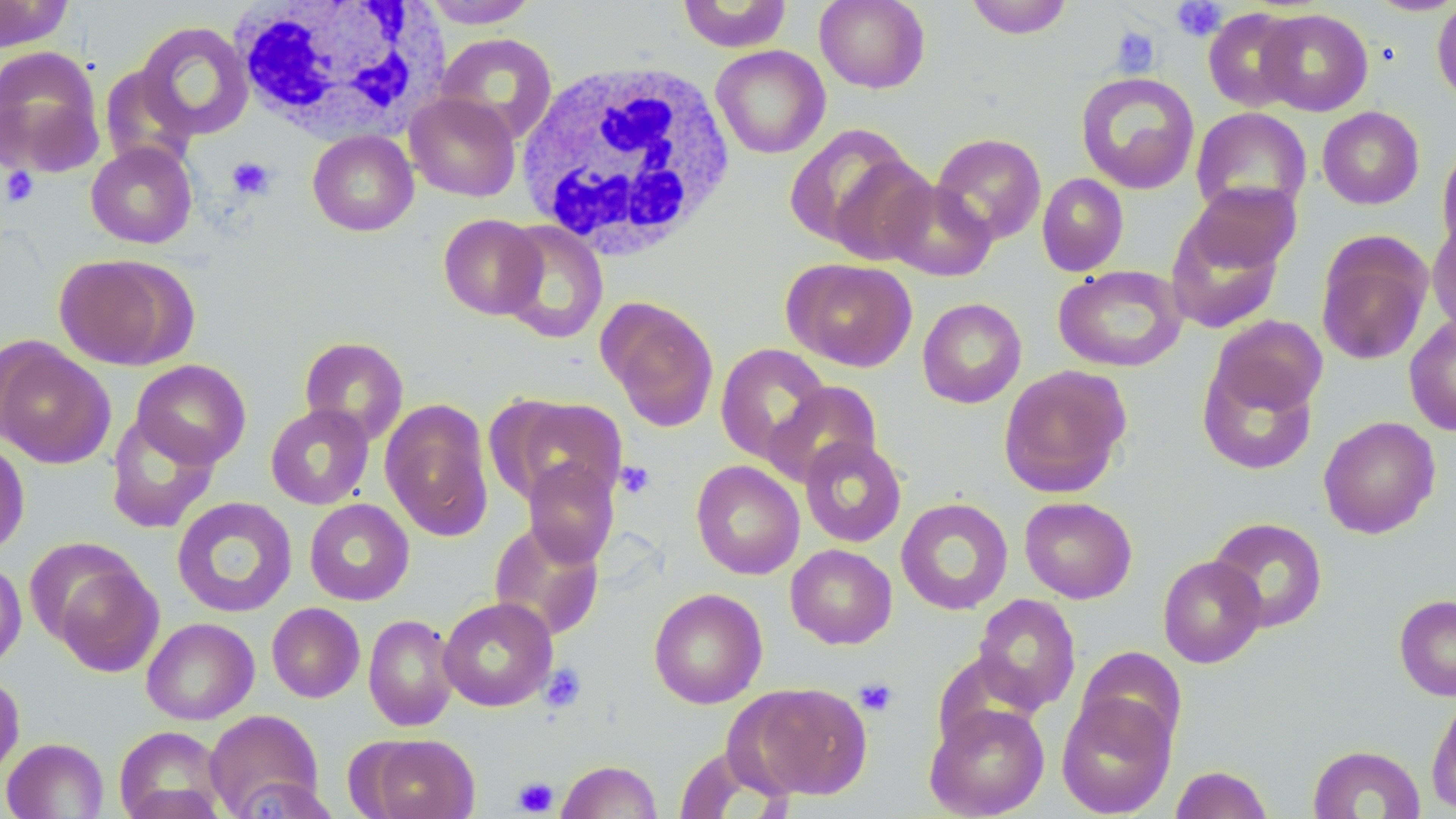
slide-level diagnosis = negative for blood parasites
white blood cell locations = approximate bounding boxes as (x1, y1, x2, y2) in pixels: (226, 0, 447, 144), (515, 57, 741, 260)
field of view = one of a larger specimen
stain = May-Grünwald-Giemsa
image size = 1456×819 pixels
magnification = 1000x
preparation = thin blood smear
uninfected red blood cell locations = approximate bounding boxes as (x1, y1, x2, y2) in pixels: (419, 0, 541, 28), (675, 0, 793, 52), (814, 0, 931, 93), (964, 0, 1074, 39), (1365, 0, 1456, 16), (1431, 0, 1456, 105), (0, 1, 73, 51), (1203, 8, 1305, 112), (1257, 9, 1373, 116), (133, 20, 255, 141), (437, 32, 558, 144), (0, 45, 105, 176), (710, 45, 831, 159), (99, 64, 199, 172), (1076, 72, 1200, 195), (405, 93, 521, 201), (1317, 106, 1424, 210), (1191, 107, 1312, 218), (784, 122, 926, 256), (307, 130, 419, 236), (931, 132, 1046, 245), (1436, 140, 1456, 258), (86, 142, 198, 248), (1037, 173, 1129, 277), (881, 179, 997, 281), (1185, 182, 1300, 277), (1165, 213, 1287, 334), (438, 214, 546, 320), (1427, 219, 1456, 338), (497, 221, 609, 344), (1315, 231, 1433, 366), (54, 254, 194, 371), (782, 258, 917, 372), (1053, 264, 1188, 372), (598, 297, 720, 432), (917, 297, 1027, 408), (1404, 314, 1456, 436), (1210, 315, 1328, 418), (298, 336, 409, 445), (0, 338, 115, 469), (715, 343, 832, 464), (1197, 358, 1318, 475), (131, 359, 251, 468), (998, 365, 1131, 498), (763, 380, 883, 488), (493, 395, 628, 509), (380, 399, 494, 542), (265, 404, 374, 510), (104, 413, 220, 534), (1318, 415, 1441, 539), (799, 436, 907, 547), (0, 437, 30, 559), (523, 459, 619, 567), (690, 460, 804, 579), (171, 496, 298, 618), (1019, 496, 1138, 604), (895, 497, 1014, 615), (304, 499, 415, 605), (1208, 517, 1328, 633), (488, 520, 605, 641), (785, 544, 897, 649), (1157, 555, 1267, 668), (45, 556, 164, 678), (0, 559, 26, 670), (648, 588, 767, 708), (972, 593, 1081, 715), (1394, 595, 1456, 701), (438, 596, 557, 711), (266, 602, 365, 703), (363, 613, 459, 731), (141, 617, 259, 724), (1076, 646, 1187, 753), (0, 672, 25, 784), (739, 683, 873, 800), (1056, 691, 1177, 818), (1426, 692, 1456, 815), (925, 702, 1050, 818), (204, 709, 325, 817), (114, 726, 226, 819), (360, 733, 480, 819), (1, 737, 109, 818), (1308, 744, 1426, 818), (556, 759, 663, 818), (1170, 765, 1273, 819), (229, 776, 340, 818)
modality = optical microscopy
platelet locations = approximate bounding boxes as (x1, y1, x2, y2) in pixels: (1171, 1, 1227, 41), (1110, 26, 1160, 78), (227, 156, 276, 199), (1, 166, 39, 207), (615, 461, 656, 499), (539, 663, 586, 712), (854, 677, 898, 717), (512, 776, 559, 816)